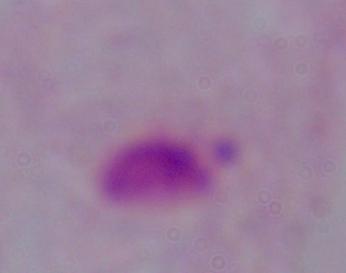

{
  "magnification": "1000x",
  "identification": "trichomonad",
  "modality": "micrograph"
}